Classify this cell by malaria status.
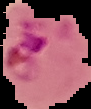
It is parasitized.

Image is 91×109 pixels. The area outside the segmented cell region is set to black. From a thin blood smear.